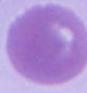

magnification: 1000x
modality: micrograph
identification: red blood cell